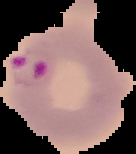

Summary:
  - Image size: 136×154 pixels
  - Image type: cell region segmented out of the field of view; surrounding area masked to black
  - Result: Plasmodium parasites detected
  - Preparation: thin blood film